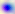
{
  "modality": "micrograph",
  "identification": "Toxoplasma gondii",
  "magnification": "400x"
}